Outline each blood parasite and name the species.
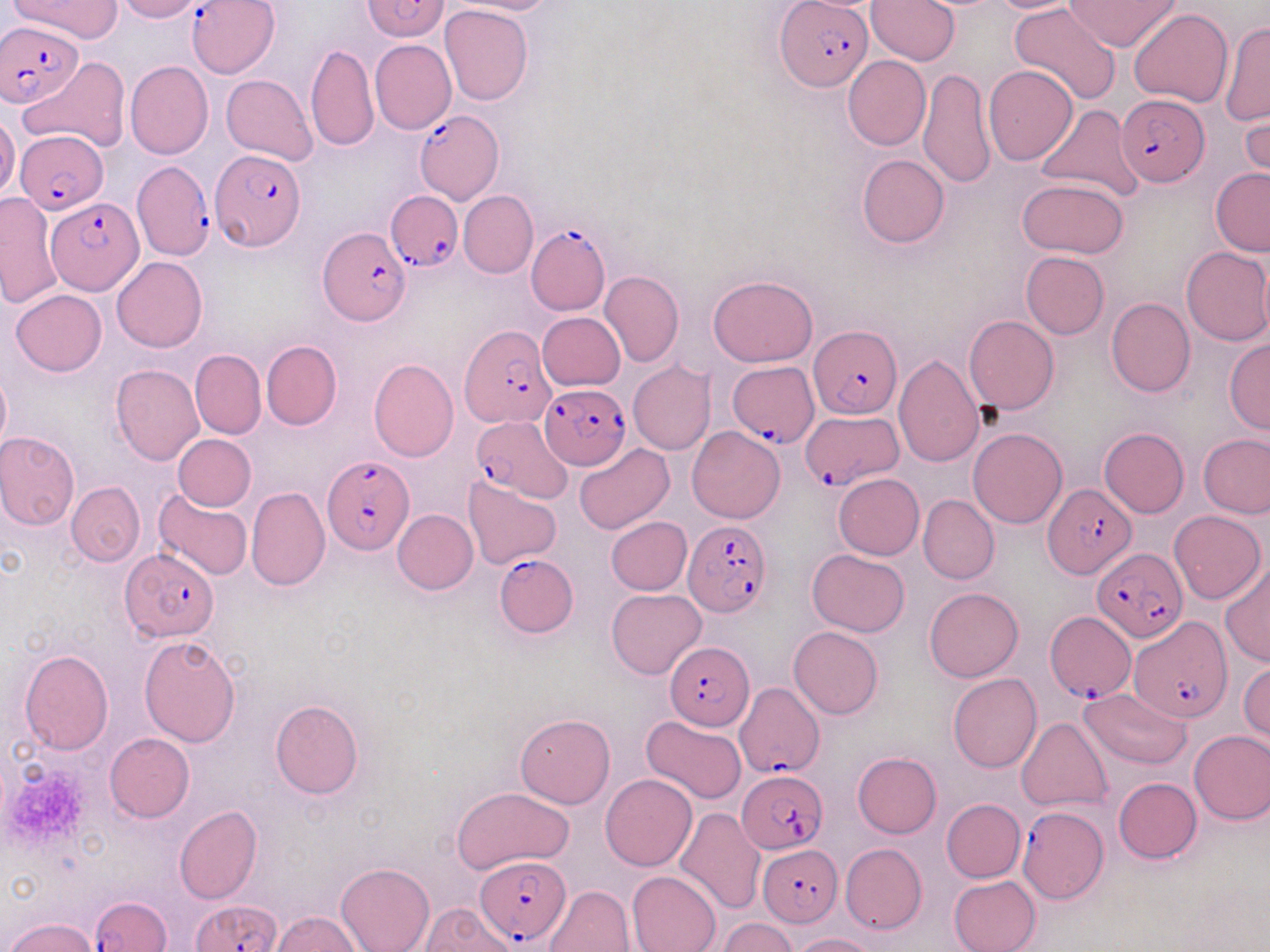
Approximate bounding boxes as [x1, y1, x2, y2] in pixels.
Plasmodium falciparum-infected red blood cells: [362, 0, 450, 42], [187, 1, 278, 77], [776, 2, 872, 90], [0, 20, 84, 108], [1117, 94, 1207, 188], [413, 109, 503, 203], [15, 135, 107, 211], [210, 148, 305, 250], [131, 161, 215, 261], [386, 193, 460, 270], [45, 196, 143, 298], [526, 225, 611, 315], [319, 226, 411, 325], [460, 323, 555, 428], [809, 325, 901, 418], [729, 360, 819, 446], [540, 383, 631, 469], [799, 411, 903, 489], [468, 417, 570, 500], [321, 453, 414, 554], [1044, 483, 1135, 578], [681, 517, 772, 617], [1091, 547, 1187, 642], [123, 548, 218, 641], [494, 553, 577, 635], [1045, 613, 1135, 704], [1132, 617, 1231, 722], [665, 641, 755, 728], [734, 681, 824, 778], [736, 770, 827, 854], [1017, 804, 1106, 903], [760, 843, 842, 926], [472, 855, 571, 945], [91, 896, 171, 952], [192, 899, 280, 952].
No Plasmodium ovale, Plasmodium malariae, Plasmodium vivax, Babesia divergens, or Trypanosoma brucei observed.

Summary:
  - Platelet locations: [4, 762, 92, 850]
  - Uninfected red blood cell locations: [10, 0, 122, 43], [114, 0, 203, 21], [445, 0, 560, 16], [867, 0, 959, 65], [987, 0, 1084, 14], [1067, 1, 1179, 50], [1010, 3, 1120, 106], [440, 4, 533, 105], [1129, 9, 1233, 108], [1220, 20, 1269, 125], [370, 40, 457, 135], [306, 44, 378, 152], [842, 56, 930, 150], [20, 57, 129, 154], [126, 61, 213, 159], [983, 65, 1079, 165], [919, 68, 994, 189], [221, 75, 318, 165], [1239, 94, 1269, 185], [1036, 105, 1145, 202], [0, 113, 20, 201], [856, 154, 949, 248], [1210, 168, 1270, 256], [1016, 178, 1129, 257], [458, 190, 538, 279], [1, 192, 61, 310], [1180, 246, 1270, 346], [1020, 251, 1109, 339], [113, 257, 207, 353], [987, 258, 1095, 371], [599, 271, 683, 369], [708, 273, 819, 367], [10, 289, 107, 376], [1106, 296, 1195, 397], [538, 311, 625, 391], [964, 314, 1059, 414], [914, 321, 1023, 437], [1224, 338, 1270, 434], [261, 340, 341, 431], [190, 348, 266, 440], [894, 354, 985, 467], [367, 358, 459, 463], [627, 361, 716, 455], [109, 363, 204, 466], [0, 367, 11, 455], [687, 426, 786, 523], [967, 427, 1068, 528], [1099, 428, 1190, 517], [0, 431, 81, 529], [173, 434, 257, 510], [1199, 434, 1270, 518], [574, 442, 674, 533], [833, 473, 924, 560], [464, 475, 561, 568], [66, 481, 145, 567], [245, 486, 330, 593], [153, 488, 253, 581], [918, 494, 999, 584], [391, 508, 478, 594], [1169, 511, 1265, 604], [606, 516, 692, 594], [807, 550, 909, 637], [1219, 564, 1270, 665], [924, 587, 1023, 682], [606, 589, 705, 679], [789, 626, 883, 719], [139, 634, 241, 747], [19, 648, 114, 755], [1239, 663, 1269, 743], [948, 673, 1042, 773], [1079, 688, 1192, 768], [270, 699, 363, 799], [515, 713, 615, 807], [641, 715, 747, 803], [1016, 716, 1113, 814], [1189, 729, 1270, 824], [105, 732, 194, 821], [852, 752, 941, 838], [600, 774, 696, 871], [1113, 777, 1202, 864], [451, 786, 573, 873], [941, 799, 1025, 882], [174, 806, 261, 905], [674, 808, 765, 916], [841, 843, 926, 933], [337, 862, 433, 952], [627, 870, 722, 952], [948, 875, 1040, 952], [545, 884, 634, 952], [420, 903, 516, 952], [272, 911, 361, 951], [6, 917, 98, 952], [719, 918, 798, 952], [790, 933, 877, 952]
  - Slide-level diagnosis: Plasmodium falciparum
  - Magnification: 1000x
  - Modality: optical microscopy
  - Stain: May-Grünwald-Giemsa
  - Image size: 1270×952 pixels
  - Preparation: thin blood film
  - Field of view: one of a larger specimen